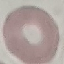
Result: no malaria parasites detected. Giemsa-stained preparation. Thin smear of blood. Photographed with a smartphone camera at the microscope eyepiece. Cell patch, automatically extracted from a larger field of view and resized to 64 × 64 pixels.